Outline platelets.
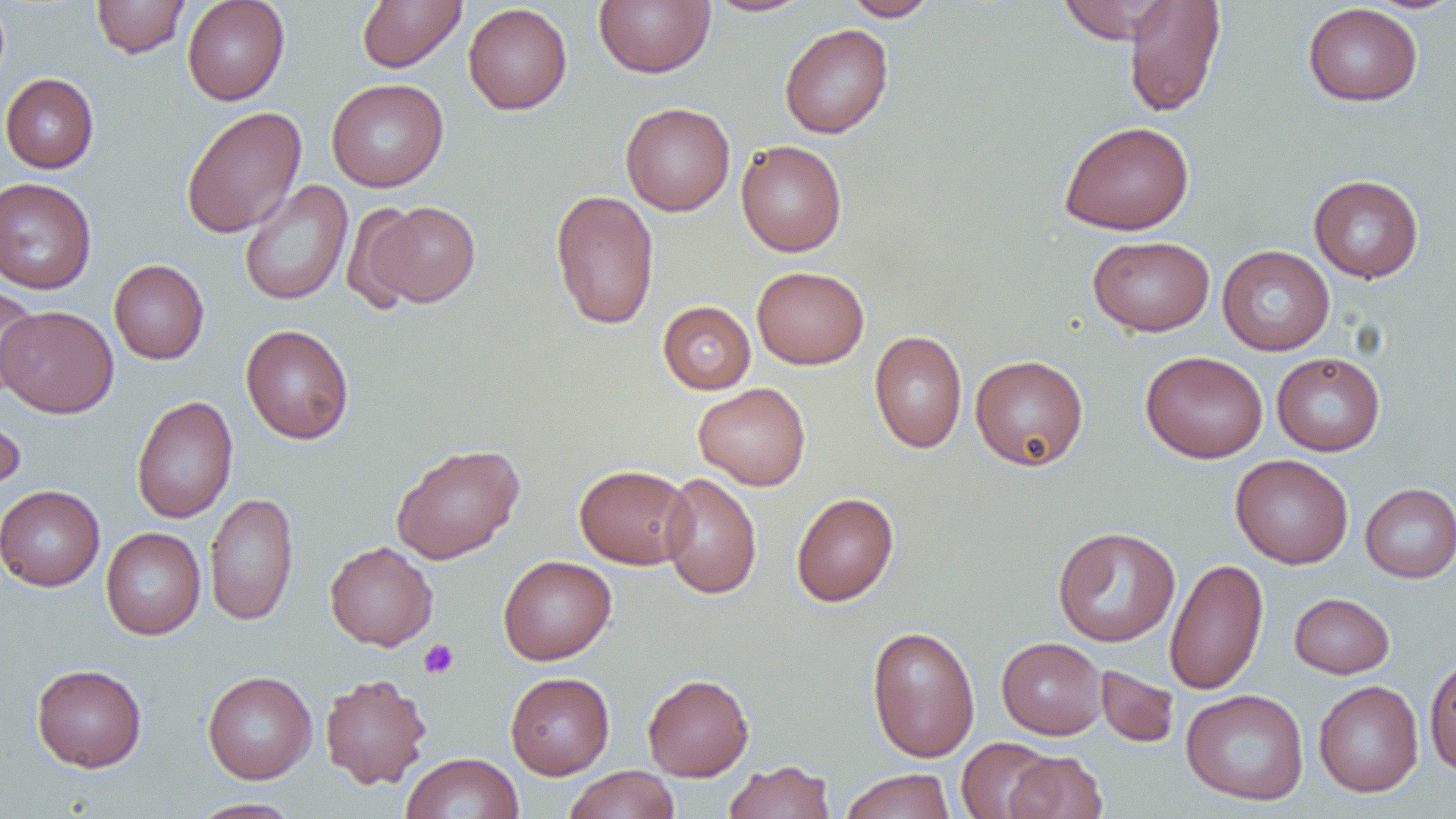
Approximate bounding boxes as [x1, y1, x2, y2] in pixels.
Platelets: [419, 639, 459, 679].

Uninfected red blood cell locations: [91, 0, 190, 58], [182, 0, 290, 106], [357, 0, 466, 73], [594, 0, 715, 78], [702, 0, 815, 17], [841, 0, 940, 21], [1055, 0, 1173, 43], [1122, 1, 1226, 117], [353, 2, 464, 151], [463, 3, 573, 115], [1303, 3, 1423, 106], [779, 23, 893, 139], [0, 73, 99, 173], [325, 78, 449, 192], [620, 102, 735, 216], [181, 105, 307, 239], [1059, 121, 1194, 235], [736, 140, 847, 257], [1308, 174, 1424, 282], [0, 177, 97, 295], [239, 179, 353, 306], [550, 189, 660, 330], [341, 201, 427, 313], [367, 201, 481, 307], [1088, 235, 1215, 336], [1217, 245, 1335, 355], [109, 259, 209, 364], [752, 266, 869, 369], [0, 287, 41, 395], [657, 301, 755, 394], [1, 305, 118, 417], [240, 324, 355, 444], [869, 331, 967, 453], [1140, 351, 1268, 463], [1272, 352, 1385, 456], [970, 355, 1089, 471], [694, 382, 811, 490], [131, 395, 238, 523], [0, 407, 25, 498], [390, 442, 525, 564], [1230, 454, 1354, 568], [574, 464, 694, 569], [660, 472, 762, 600], [1360, 482, 1456, 583], [0, 485, 105, 591], [205, 492, 299, 627], [791, 492, 899, 606], [1052, 526, 1180, 647], [101, 528, 205, 640], [324, 541, 438, 650], [498, 555, 616, 664], [1164, 557, 1268, 695], [1289, 592, 1395, 678], [866, 625, 980, 762], [997, 636, 1107, 739], [1424, 653, 1456, 776], [31, 663, 147, 771], [1095, 665, 1180, 748], [202, 670, 317, 783], [319, 672, 432, 790], [505, 672, 615, 779], [642, 673, 754, 780], [1313, 680, 1423, 798], [1181, 688, 1309, 806], [956, 737, 1059, 819], [1004, 751, 1108, 819], [401, 752, 524, 819], [723, 759, 836, 819], [564, 765, 679, 819], [839, 768, 956, 819], [188, 798, 300, 819]. Slide-level diagnosis: no evidence of blood parasites. Image is 1456×819 pixels. 1000x magnification. Light microscopy. One field of a larger specimen. Thin blood film.